Classify this cell by malaria status.
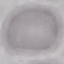
It is uninfected.

Thin smear of blood. Acquired by smartphone through the microscope eyepiece. Giemsa stain. Cell patch, automatically extracted from a larger field of view and resized to 64 × 64 pixels.